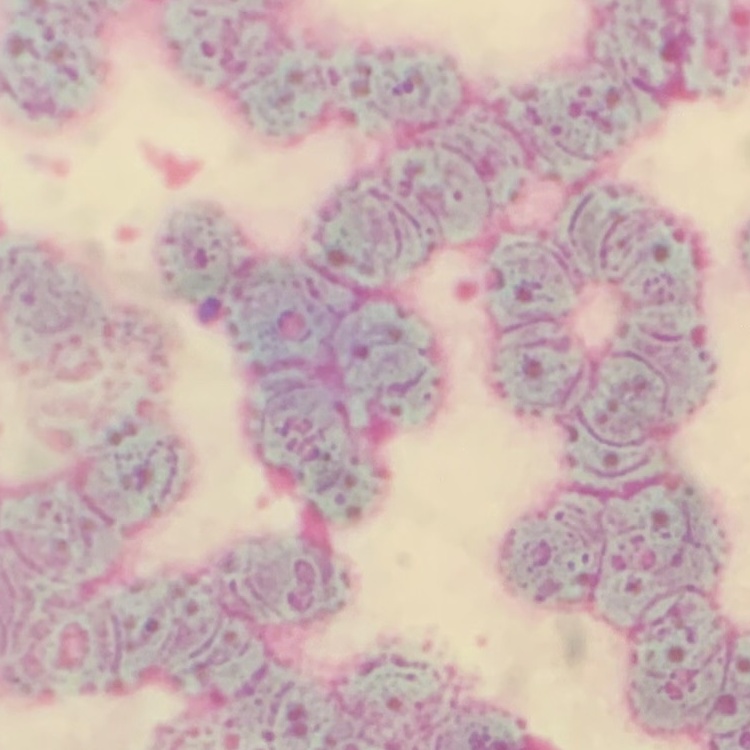

The red blood cells exhibit rouleaux formation. Field's or Giemsa stain. Thin blood film. One tile cut from a larger photomicrograph.